Describe the morphology of the red blood cells.
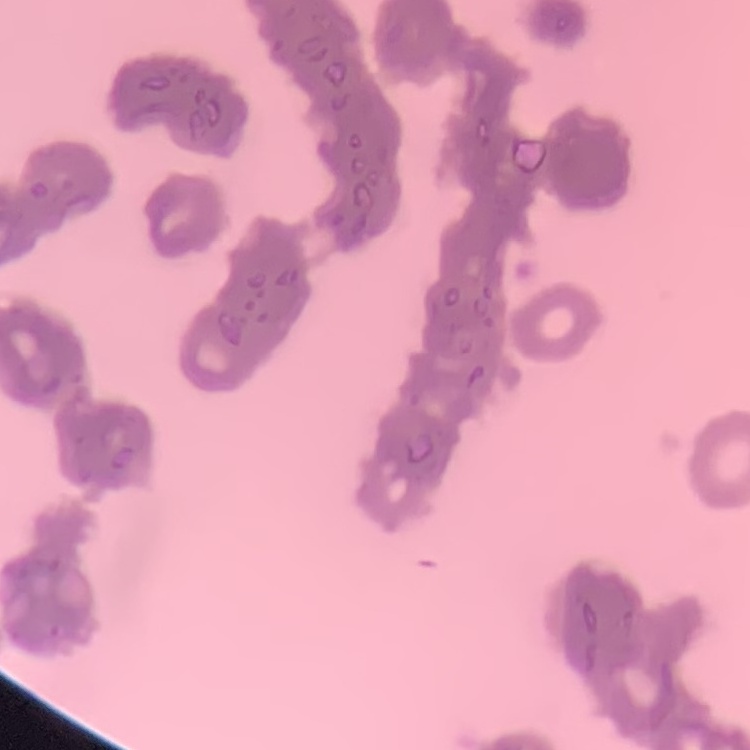

They show rouleaux formation.

image type = one tile cut from a larger photomicrograph
stain = Field's or Giemsa
preparation = thin blood smear